Give the position of every Plasmodium parasite visible.
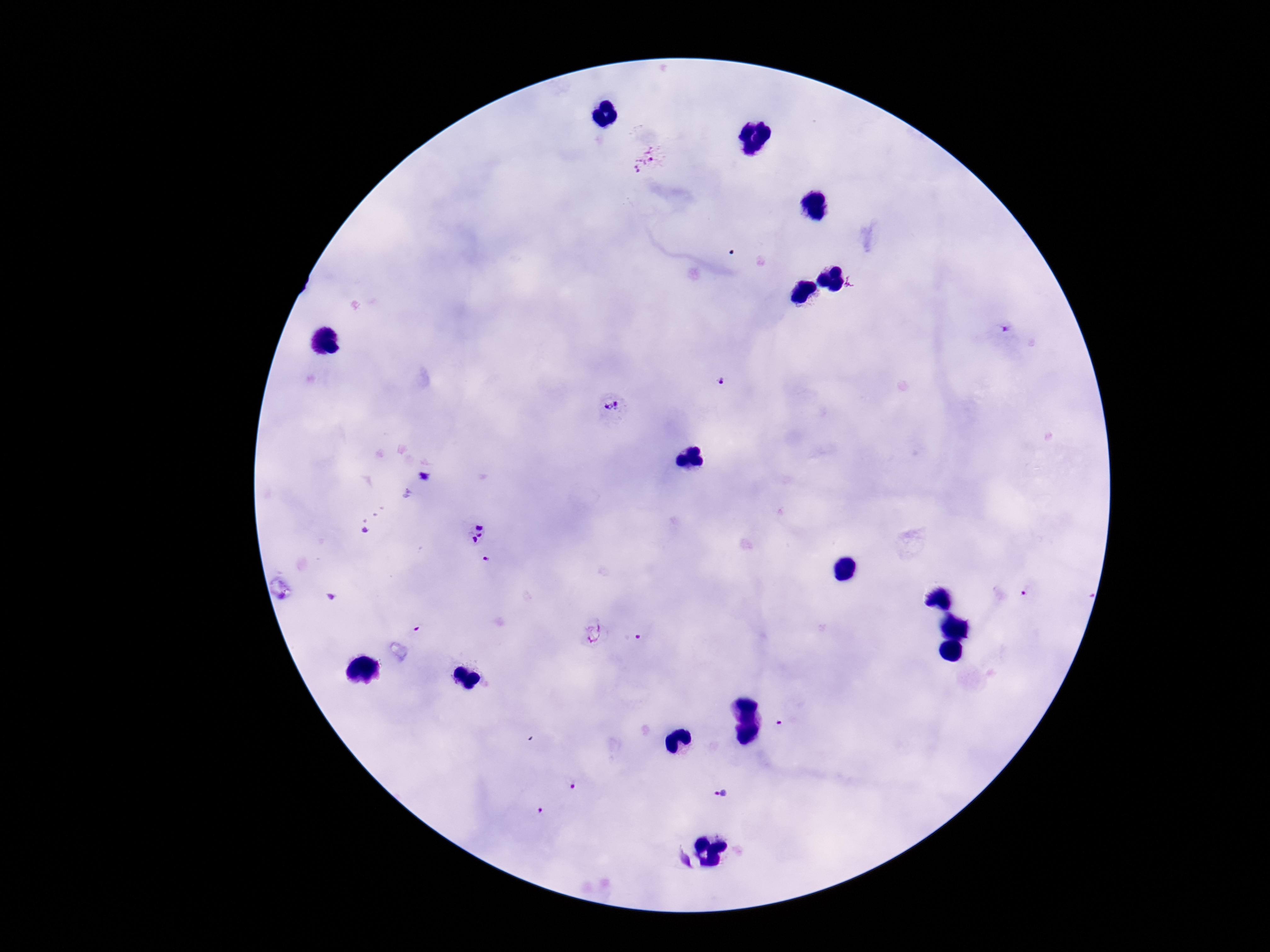
Approximate centers as {x, y} in pixels.
Plasmodium parasites: {650, 159}, {1004, 328}, {722, 383}, {611, 410}, {422, 477}, {470, 531}, {366, 533}, {486, 561}, {1026, 593}, {419, 628}, {595, 635}, {637, 637}, {782, 725}, {574, 787}, {722, 792}, {542, 810}.

Summary:
  - Field of view: single
  - Image size: 1270×952 pixels
  - Preparation: thick peripheral-blood smear
  - Stain: Giemsa
  - Magnification: 100x
  - Capture: smartphone camera through the microscope eyepiece
  - Patient malaria status: infected